Draw a bounding box around every trophozoite.
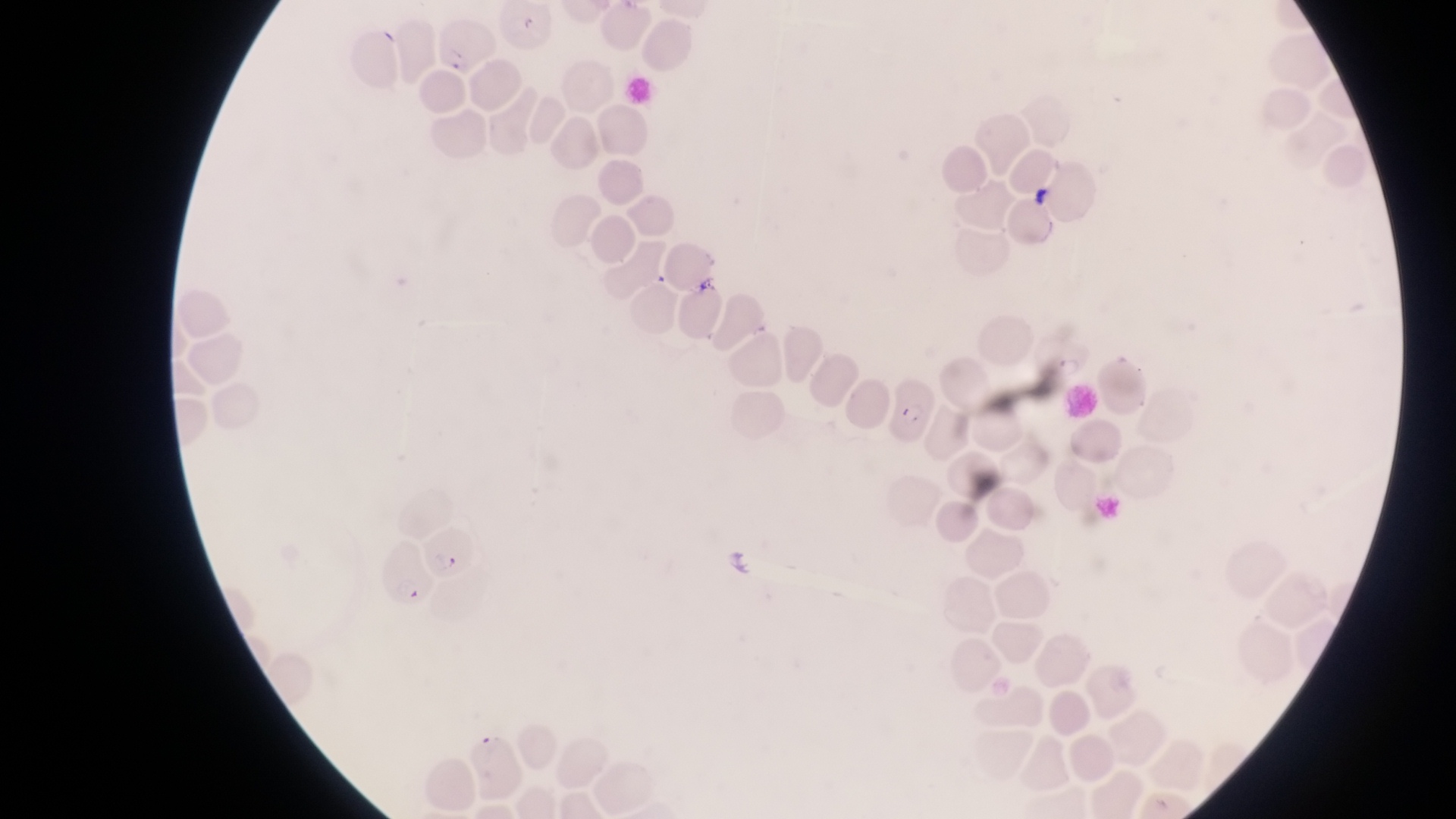

Approximate bounding boxes as left top right bottom in pixels.
Trophozoites: 1047 350 1093 384.

country = Uganda
field of view = single
image size = 1456×819 pixels
parasitised red blood cell locations = approximate bounding boxes as left top right bottom in pixels: 428 19 491 71; 890 375 935 446; 422 525 477 581; 376 541 435 604
preparation = thin blood smear
artifact (platelet-like body, stain precipitate, or debris) locations = approximate bounding boxes as left top right bottom in pixels: 1027 180 1057 216; 697 268 721 294
capture = smartphone photograph through the eyepiece of an Olympus CX-23 microscope
magnification = 1000x